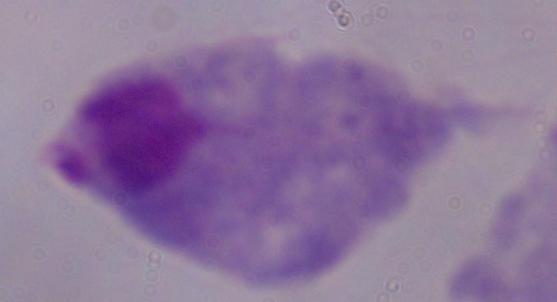

magnification = 1000x
identification = trichomonad
modality = photomicrograph